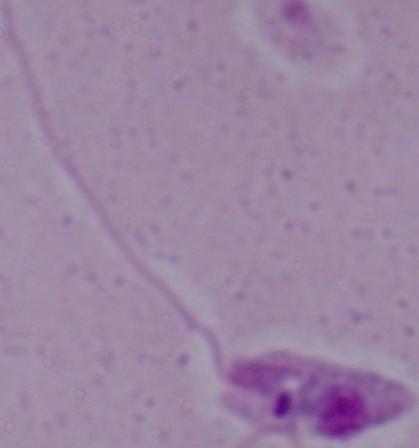

Photomicrograph. Captured at 1000x magnification. A Leishmania parasite is shown.